Point out each Plasmodium parasite.
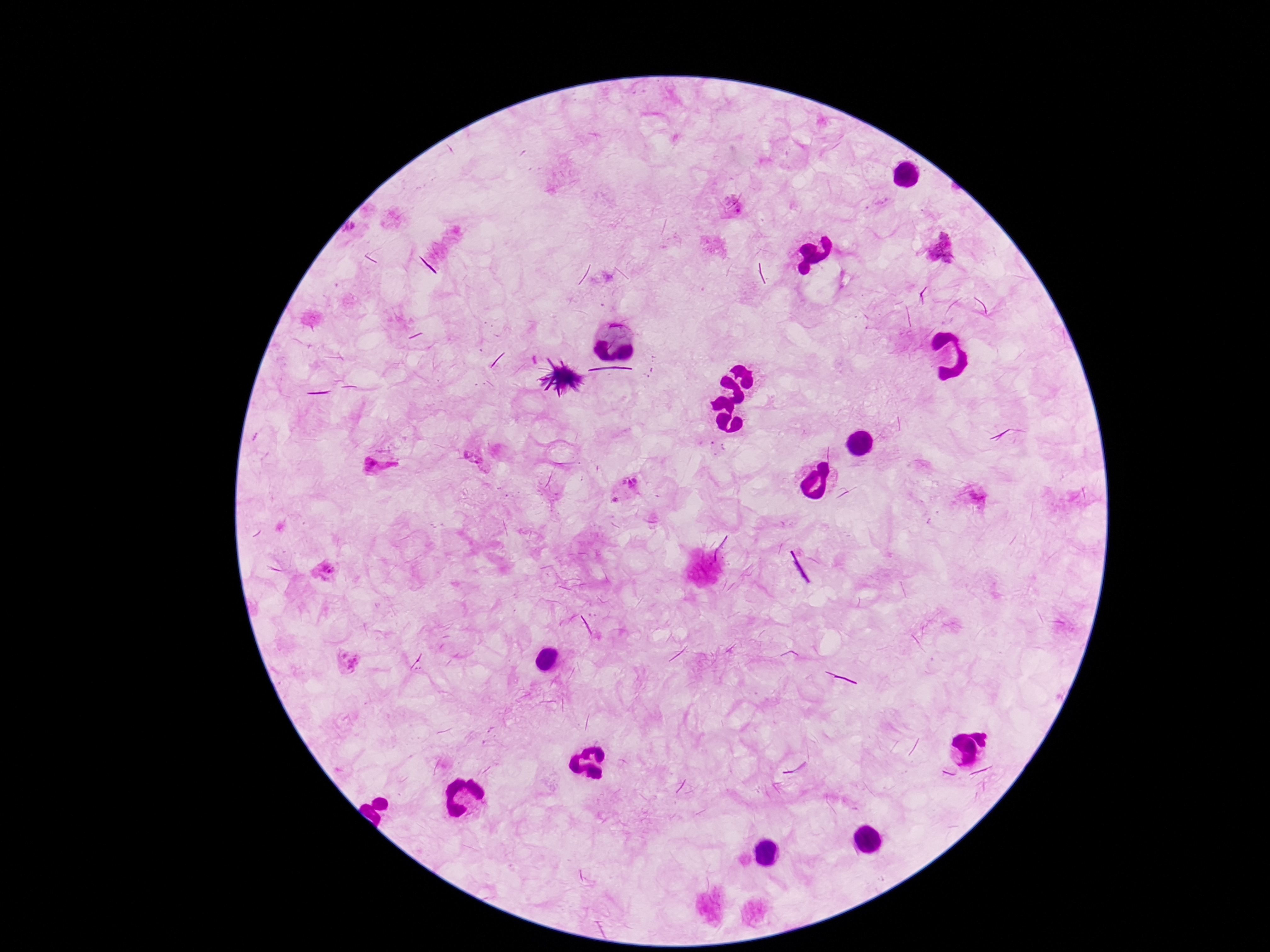

Approximate centers as [x, y] in pixels.
Plasmodium parasites: [738, 205], [944, 249], [717, 447], [477, 461], [378, 468], [629, 484], [617, 497], [981, 499], [325, 570], [349, 660].

{
  "stain": "Giemsa",
  "capture": "smartphone camera through the microscope eyepiece",
  "preparation": "thick blood film",
  "magnification": "100x",
  "patient_malaria_status": "positive",
  "field_of_view": "single",
  "image_size": "1270×952 pixels"
}